Report the malaria status of this cell.
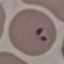
It is parasitized.

image type = automatically extracted cell patch, resized to 64 × 64 pixels
capture = smartphone through the microscope eyepiece
stain = Giemsa
preparation = thin blood film